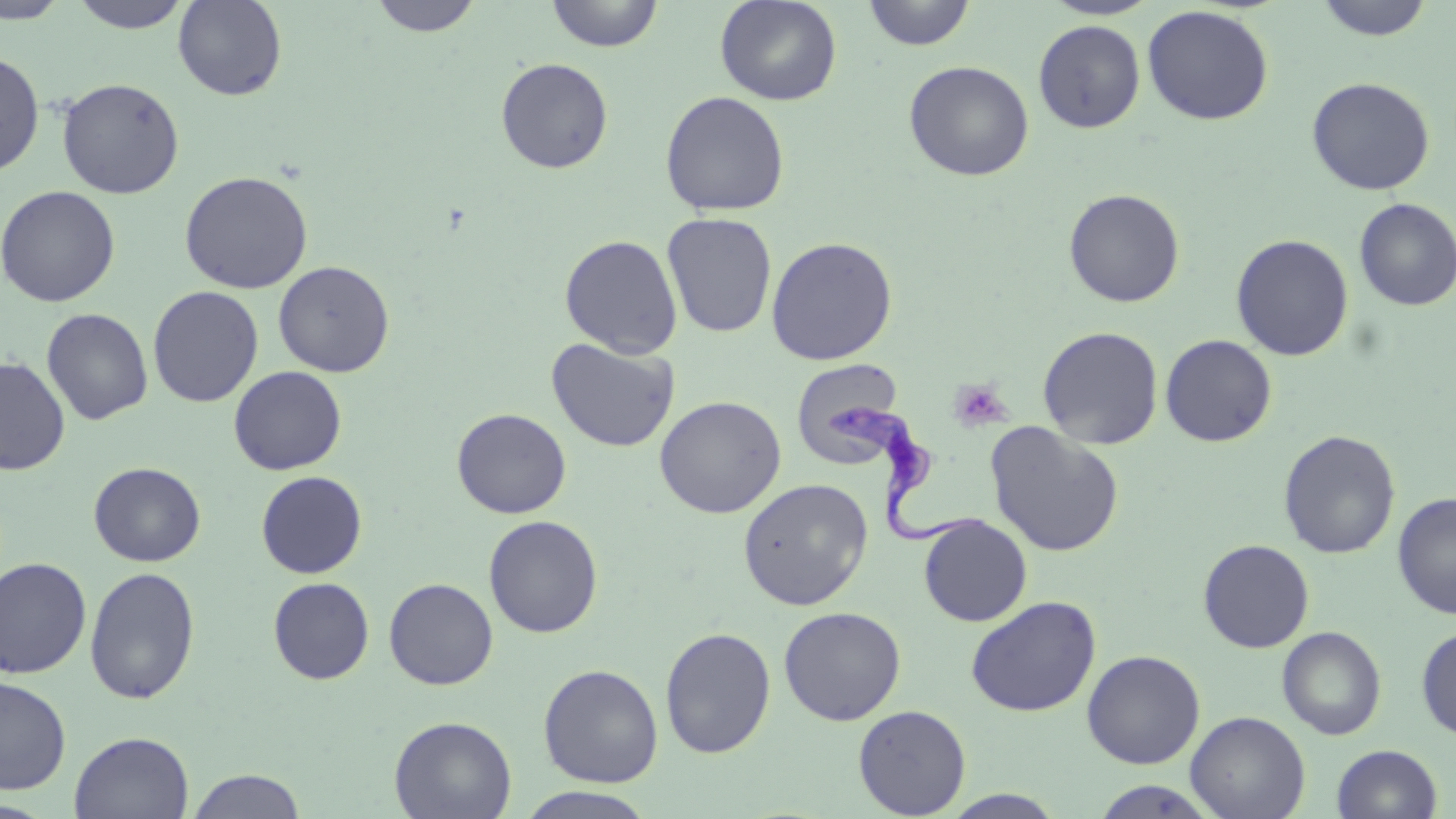
Summary:
  - Coordinate format: approximate bounding boxes as (x1, y1, x2, y2) in pixels
  - Uninfected red blood cell locations: (0, 0, 71, 24), (67, 0, 194, 33), (173, 0, 287, 101), (368, 0, 484, 37), (546, 0, 664, 52), (714, 0, 843, 106), (1041, 0, 1160, 20), (1314, 0, 1435, 42), (862, 1, 975, 51), (1142, 5, 1274, 125), (1033, 19, 1145, 133), (0, 50, 44, 177), (495, 57, 613, 174), (903, 60, 1034, 181), (1306, 77, 1435, 196), (57, 78, 184, 199), (659, 90, 790, 216), (179, 170, 314, 293), (0, 185, 120, 307), (1063, 188, 1185, 307), (1354, 198, 1456, 311), (662, 213, 778, 338), (1230, 233, 1354, 361), (559, 234, 683, 358), (765, 236, 898, 365), (273, 260, 395, 377), (147, 286, 264, 408), (41, 308, 153, 425), (1037, 325, 1164, 449), (1159, 334, 1277, 447), (546, 337, 681, 452), (0, 357, 70, 475), (790, 360, 909, 469), (228, 366, 347, 476), (654, 395, 786, 518), (452, 407, 571, 518), (985, 422, 1125, 558), (1279, 429, 1401, 559), (89, 462, 206, 567), (256, 470, 367, 578), (737, 478, 873, 610), (1393, 492, 1456, 619), (483, 515, 603, 638), (919, 515, 1032, 627), (1197, 539, 1315, 653), (0, 557, 93, 678), (84, 566, 200, 704), (268, 577, 375, 685), (384, 578, 498, 690), (965, 595, 1101, 717), (778, 606, 906, 725), (1416, 625, 1456, 741), (660, 626, 776, 758), (1277, 626, 1386, 740), (1082, 650, 1205, 769), (538, 663, 663, 787), (0, 675, 71, 795), (853, 704, 972, 818), (1185, 710, 1311, 819), (389, 715, 517, 819), (69, 731, 194, 819), (1331, 744, 1442, 819), (185, 768, 307, 818), (1088, 779, 1222, 819), (515, 786, 658, 819), (940, 790, 1067, 818)
  - Platelet locations: (949, 378, 1012, 432)
  - Trypanosoma brucei locations: (825, 401, 993, 554)
  - Slide-level diagnosis: Trypanosoma brucei
  - Field of view: single
  - Preparation: thin blood film
  - Modality: light microscopy
  - Image size: 1456×819 pixels
  - Magnification: 1000x
  - Stain: May-Grünwald-Giemsa